Identify the parasite.
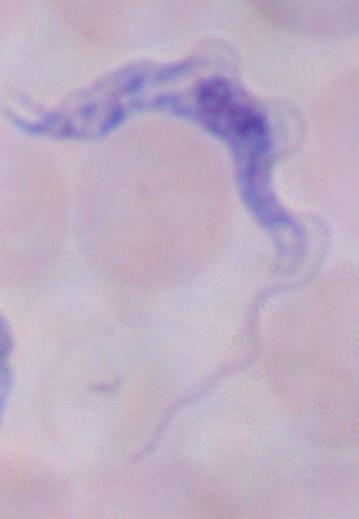
A trypanosome.

Micrograph. 1000x magnification.